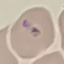

Malaria status: uninfected. Automatically extracted cell patch, resized to 64 × 64 pixels. Thin blood film. Giemsa-stained preparation. Acquired by smartphone through the microscope eyepiece.